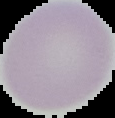 Segmented cell region on a black background. Image is 115×118 pixels. Malaria status: uninfected. From a thin blood film.